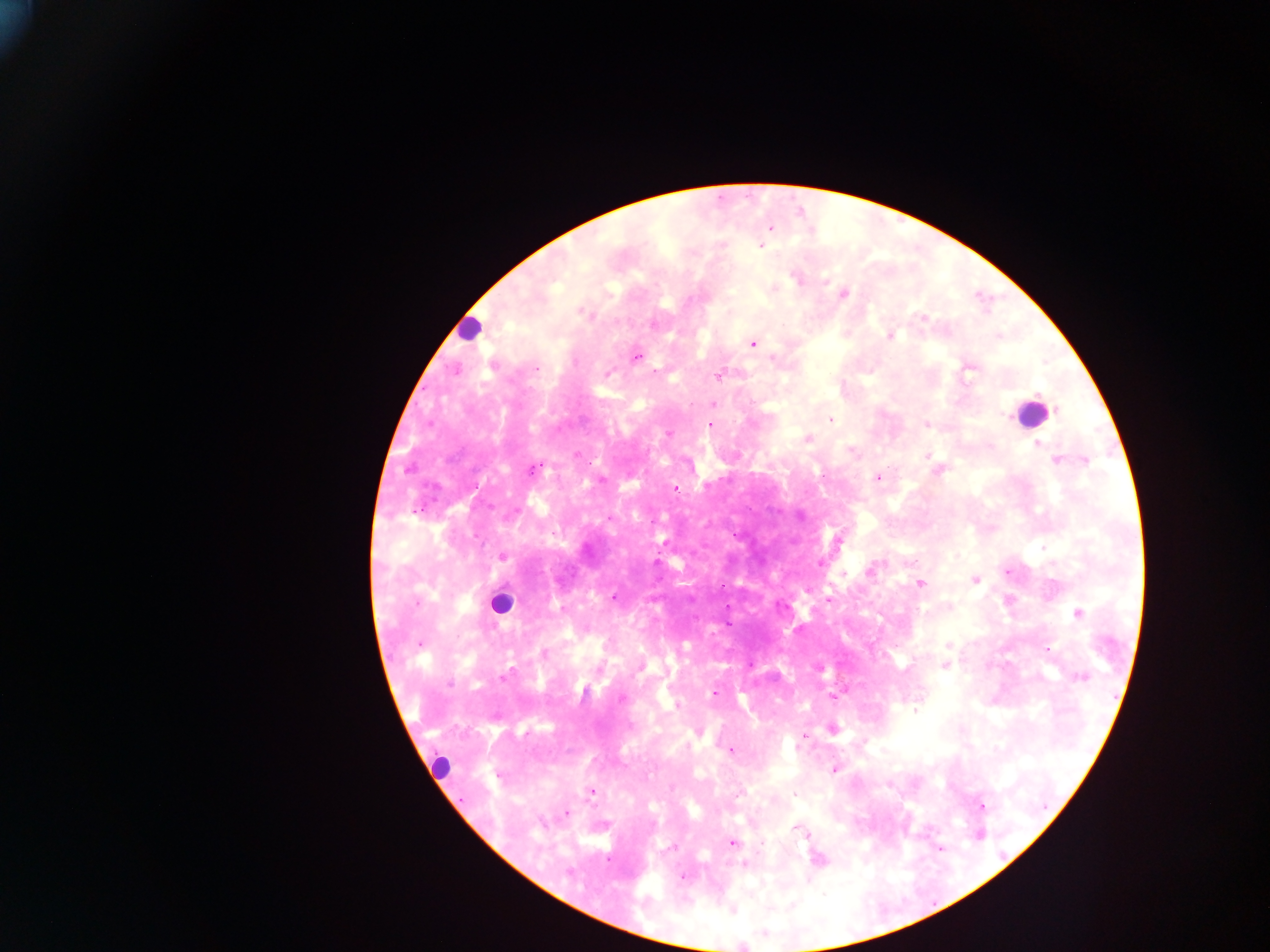
Approximate centers as {x, y} in pixels. Malaria parasite locations: {770, 229}, {760, 246}, {796, 278}, {825, 281}, {844, 294}, {583, 313}, {924, 318}, {653, 325}, {890, 336}, {752, 344}, {637, 358}, {772, 359}, {536, 369}, {970, 369}, {655, 371}, {607, 373}, {719, 376}, {1039, 396}, {713, 405}, {1057, 410}, {1003, 414}, {831, 419}, {710, 424}, {925, 425}, {669, 433}, {808, 438}, {1038, 444}, {990, 446}, {927, 455}, {1056, 460}, {1086, 461}, {535, 468}, {939, 470}, {877, 477}, {675, 489}, {800, 516}, {610, 518}, {838, 540}, {1044, 547}, {502, 556}, {819, 564}, {870, 571}, {1007, 571}, {843, 575}, {974, 580}, {919, 583}, {614, 597}, {829, 600}, {561, 609}, {1078, 613}, {419, 644}, {948, 645}, {1048, 649}, {545, 653}, {945, 666}, {639, 668}, {506, 674}, {1082, 676}, {449, 684}, {714, 693}, {832, 696}, {621, 698}, {677, 706}, {916, 711}, {833, 730}, {804, 736}, {731, 751}, {834, 769}, {591, 791}, {738, 794}, {794, 794}, {982, 807}, {567, 814}, {542, 824}, {799, 830}, {804, 833}, {732, 843}, {819, 860}, {745, 864}, {683, 877}. Leukocyte locations: {467, 328}, {1031, 416}, {500, 603}, {440, 766}. Photographed through a microscope with a mobile-phone camera. One field of view. Thick blood smear. Sample from Ghana. Image is 1270×952 pixels.